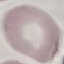
malaria status = uninfected
capture = smartphone through the microscope eyepiece
preparation = thin smear
image type = cell patch, automatically extracted from a larger field of view and resized to 64 × 64 pixels
stain = Giemsa